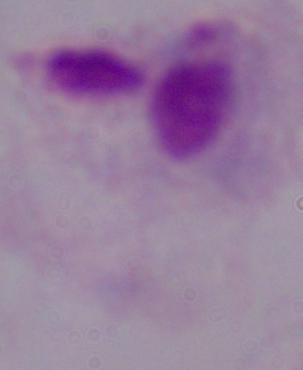
Captured at 1000x magnification. Photomicrograph. A trichomonad is seen.